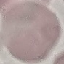
malaria status = uninfected
capture = smartphone through the microscope eyepiece
stain = Giemsa
image type = automatically extracted cell patch, resized to 64 × 64 pixels
preparation = thin smear